Locate every malaria parasite.
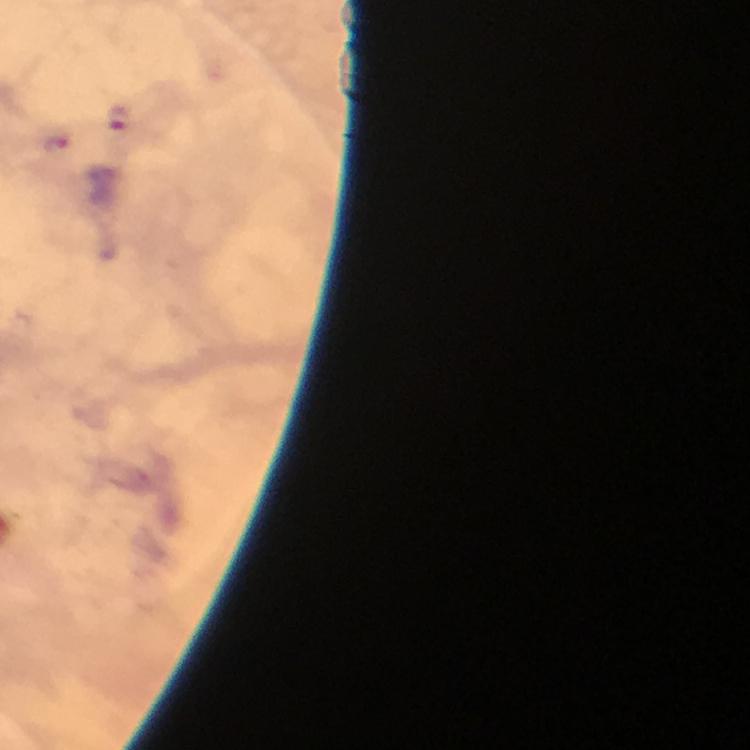
Approximate centers as [x, y] in pixels.
Malaria parasites: [118, 120], [55, 142].

image size = 750×750 pixels
context = from a malaria diagnostic workup
magnification = 100x
stain = Giemsa
cropped from = one field of view
capture = smartphone photograph through a microscope
preparation = thick blood smear
immersion oil = used